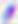
400x magnification. Toxoplasma gondii is shown. Photomicrograph.